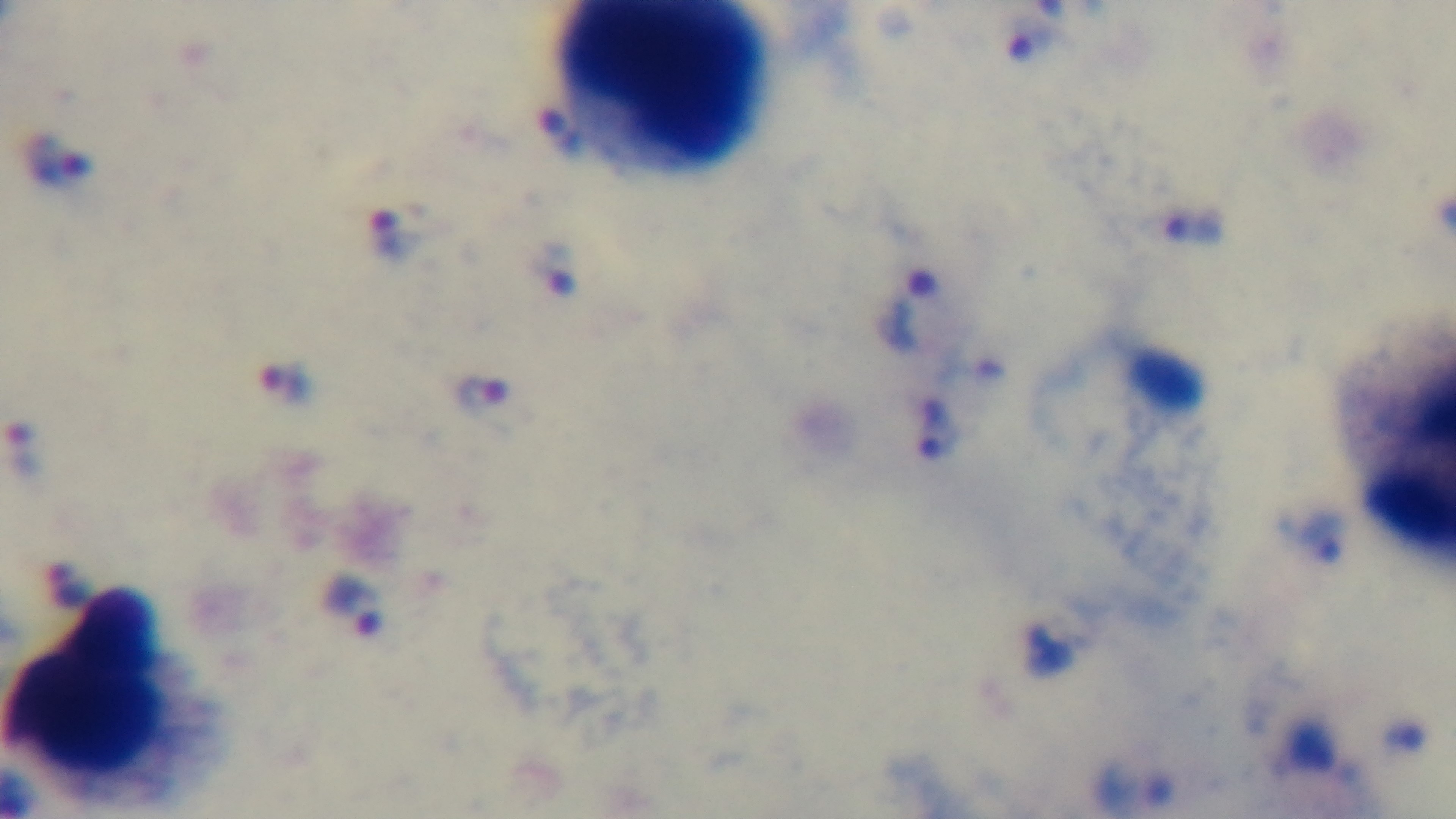

Summary:
  - Capture: mounted 4K digital camera
  - Field of view: single
  - Preparation: thick
  - Stain: Giemsa
  - Objective: 100x oil immersion
  - Modality: light microscopy
  - Malaria status: positive